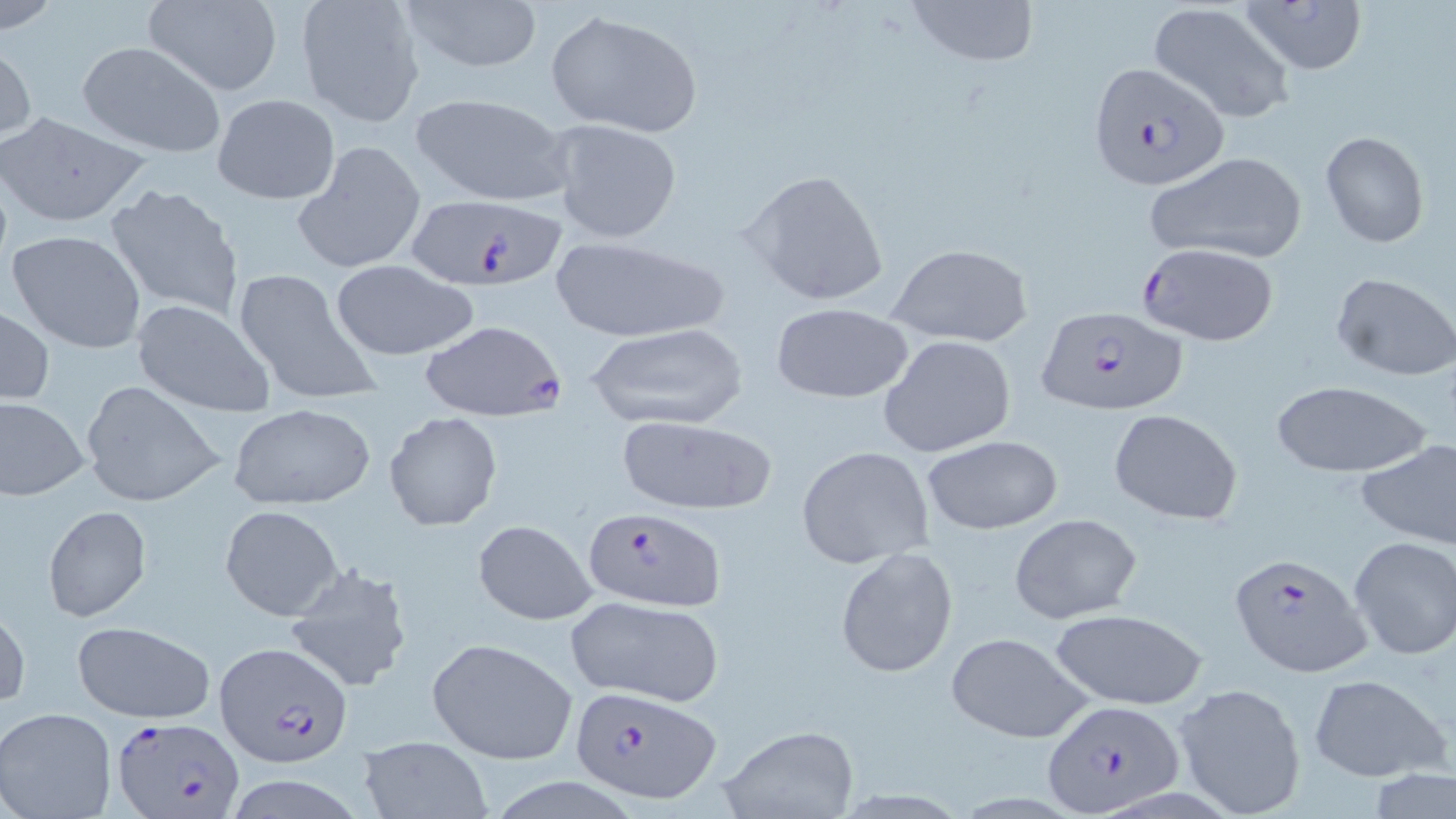

Approximate bounding boxes as named x1/y1/x2/y2 corners in pixels. Plasmodium falciparum-infected red blood cell locations: (x1=1087, y1=61, x2=1231, y2=192), (x1=406, y1=194, x2=570, y2=292), (x1=1137, y1=244, x2=1281, y2=345), (x1=1036, y1=306, x2=1187, y2=415), (x1=421, y1=319, x2=568, y2=420), (x1=584, y1=506, x2=728, y2=610), (x1=1229, y1=550, x2=1372, y2=679), (x1=214, y1=641, x2=353, y2=768), (x1=569, y1=686, x2=721, y2=803), (x1=1041, y1=699, x2=1185, y2=816), (x1=112, y1=712, x2=244, y2=819). Uninfected red blood cell locations: (x1=141, y1=0, x2=284, y2=96), (x1=391, y1=0, x2=547, y2=75), (x1=906, y1=0, x2=1041, y2=70), (x1=1240, y1=0, x2=1369, y2=75), (x1=1, y1=1, x2=63, y2=34), (x1=295, y1=1, x2=427, y2=129), (x1=1150, y1=2, x2=1295, y2=124), (x1=545, y1=9, x2=703, y2=137), (x1=77, y1=41, x2=227, y2=160), (x1=0, y1=42, x2=37, y2=146), (x1=410, y1=92, x2=573, y2=207), (x1=211, y1=93, x2=340, y2=205), (x1=0, y1=109, x2=150, y2=229), (x1=551, y1=118, x2=684, y2=245), (x1=1320, y1=130, x2=1429, y2=248), (x1=290, y1=141, x2=429, y2=276), (x1=1146, y1=150, x2=1308, y2=264), (x1=743, y1=168, x2=891, y2=307), (x1=104, y1=179, x2=245, y2=323), (x1=6, y1=228, x2=147, y2=353), (x1=550, y1=236, x2=729, y2=342), (x1=887, y1=244, x2=1034, y2=347), (x1=328, y1=258, x2=480, y2=362), (x1=231, y1=266, x2=382, y2=408), (x1=1331, y1=272, x2=1456, y2=381), (x1=132, y1=299, x2=276, y2=418), (x1=769, y1=300, x2=916, y2=404), (x1=0, y1=305, x2=54, y2=408), (x1=584, y1=322, x2=751, y2=431), (x1=878, y1=334, x2=1017, y2=460), (x1=1268, y1=379, x2=1434, y2=478), (x1=80, y1=380, x2=226, y2=506), (x1=0, y1=396, x2=89, y2=499), (x1=228, y1=402, x2=376, y2=511), (x1=1107, y1=410, x2=1243, y2=524), (x1=384, y1=411, x2=502, y2=531), (x1=614, y1=413, x2=778, y2=518), (x1=920, y1=434, x2=1064, y2=535), (x1=1355, y1=439, x2=1456, y2=550), (x1=795, y1=446, x2=934, y2=569), (x1=42, y1=504, x2=151, y2=622), (x1=219, y1=504, x2=345, y2=621), (x1=1008, y1=513, x2=1143, y2=624), (x1=472, y1=519, x2=597, y2=626), (x1=1348, y1=536, x2=1456, y2=660), (x1=835, y1=546, x2=960, y2=679), (x1=283, y1=562, x2=415, y2=694), (x1=566, y1=595, x2=724, y2=708), (x1=0, y1=605, x2=29, y2=710), (x1=1049, y1=607, x2=1209, y2=710), (x1=70, y1=620, x2=215, y2=723), (x1=945, y1=631, x2=1095, y2=744), (x1=426, y1=637, x2=578, y2=766), (x1=1305, y1=673, x2=1451, y2=784), (x1=1171, y1=681, x2=1309, y2=819), (x1=0, y1=708, x2=116, y2=819), (x1=718, y1=725, x2=859, y2=818), (x1=357, y1=734, x2=494, y2=818), (x1=1368, y1=769, x2=1452, y2=819). Slide-level diagnosis: Plasmodium falciparum. Captured at 1000x magnification. One field of a larger specimen. May-Grünwald-Giemsa-stained preparation. Light microscopy. Image is 1456×819 pixels. Thin blood film.